State the preparation type.
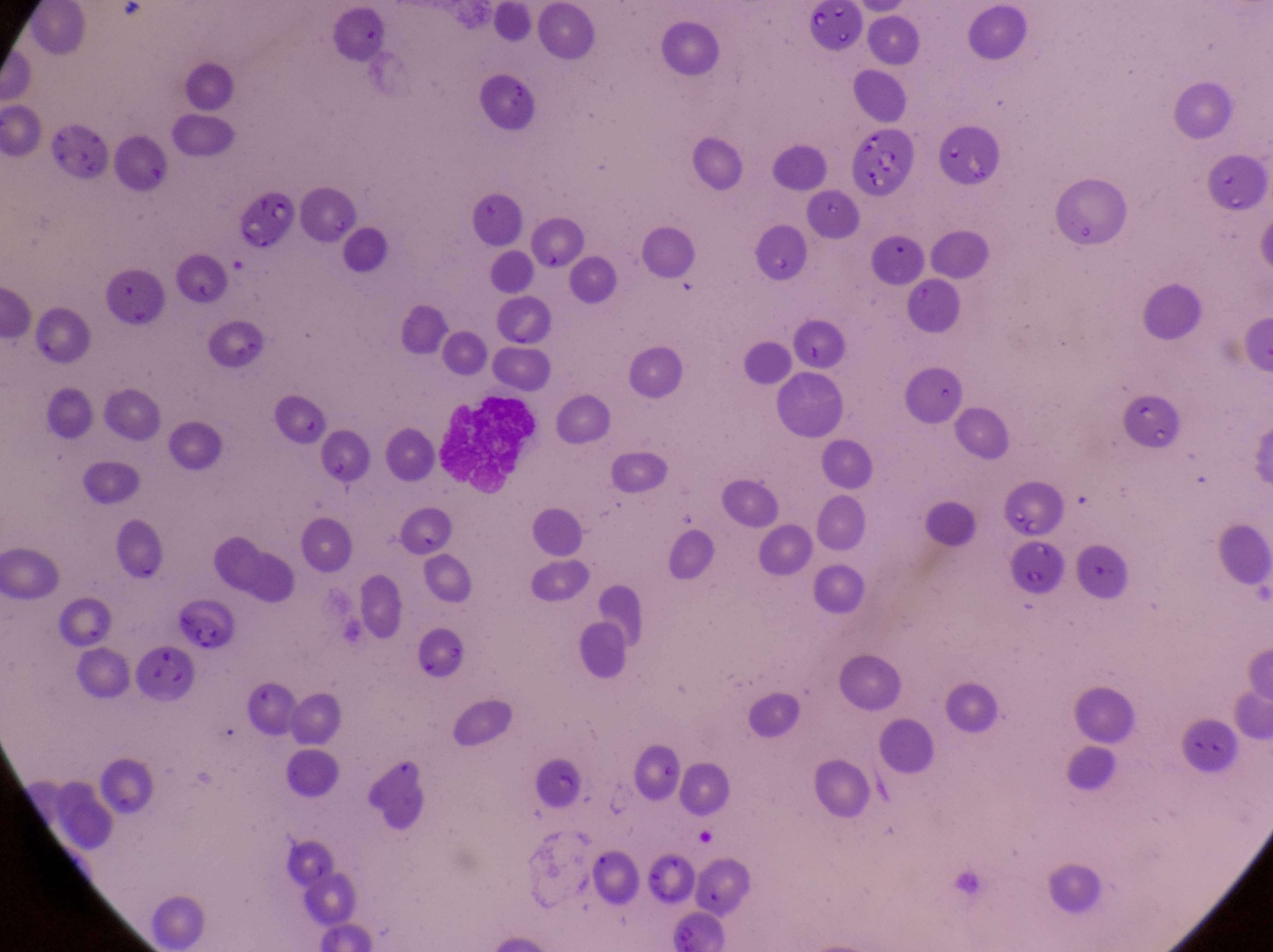
Thin blood film.

field_of_view: single
capture: smartphone photograph through the eyepiece of an Olympus CX-23 microscope
leukocyte_locations: 'approximate bounding boxes as {left, top, right, bottom} in pixels: {434, 394, 536, 506}'
artifact_platelet_like_body_stain_precipitate_or_debris_locations: 'approximate bounding boxes as {left, top, right, bottom} in pixels: {52, 112, 109, 177}, {851, 127, 916, 199}, {235, 192, 297, 245}, {272, 404, 325, 444}, {1013, 540, 1068, 598}, {167, 597, 230, 652}, {137, 642, 195, 700}'
magnification: 1000x
image_size: 1273×952 pixels
country: Uganda